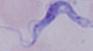 Photomicrograph. A trypanosome is seen. Captured at 1000x magnification.